Report the malaria status of this cell.
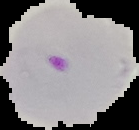

Parasitized.

Summary:
  - Image size: 139×130 pixels
  - Preparation: thin blood smear
  - Image type: cell region segmented out of the field of view; surrounding area masked to black